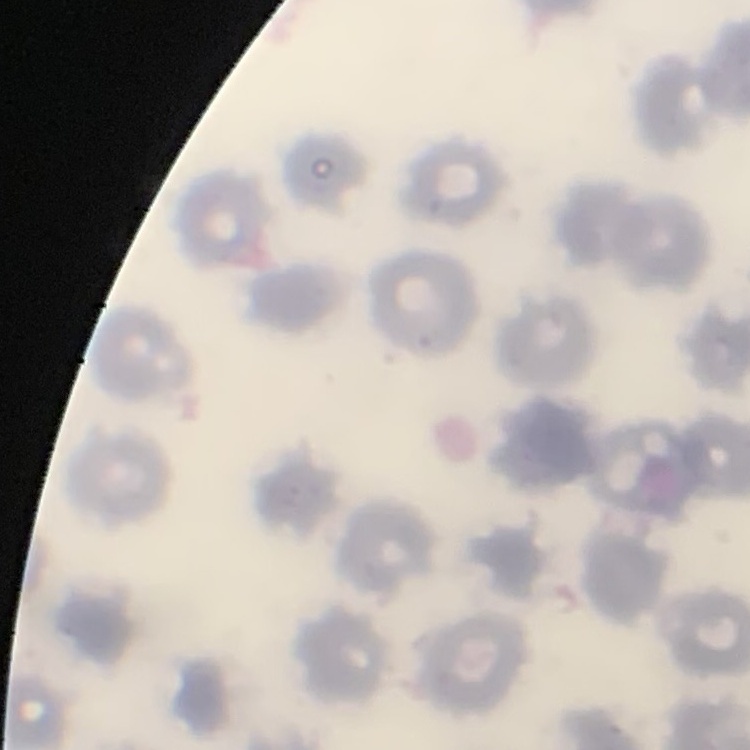
erythrocyte_morphology: no rouleaux formation
stain: Field's or Giemsa
preparation: thin blood smear
image_type: square crop of a larger photomicrograph